Point out each leukocyte.
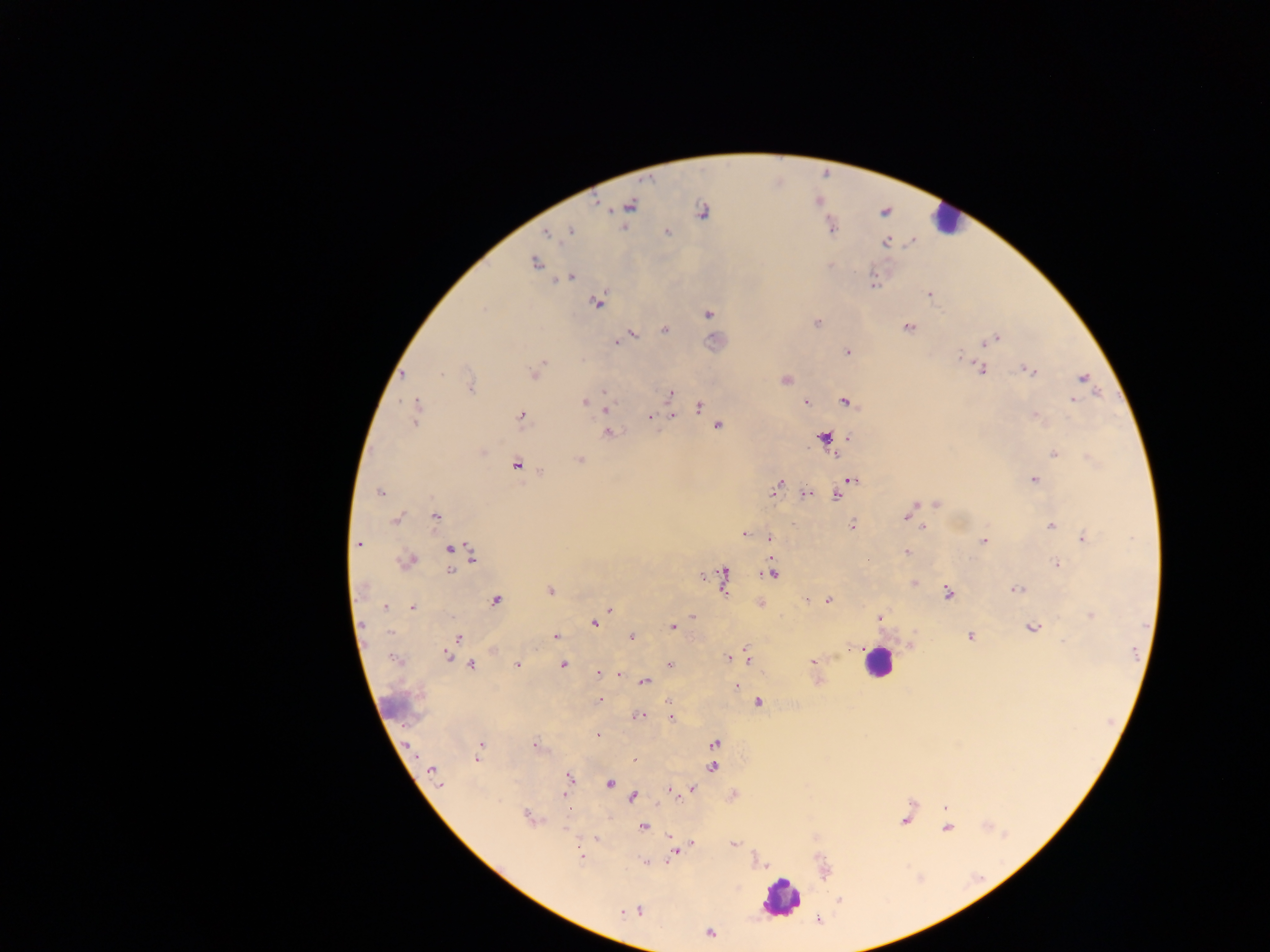

Approximate centers as {x, y} in pixels.
Leukocytes: {947, 219}, {878, 662}, {781, 897}.

Summary:
  - Malaria parasite locations: {596, 204}, {629, 205}, {701, 211}, {831, 226}, {570, 230}, {547, 231}, {667, 232}, {885, 241}, {912, 242}, {535, 262}, {570, 277}, {873, 283}, {930, 294}, {596, 302}, {708, 314}, {816, 323}, {907, 327}, {664, 329}, {631, 334}, {994, 338}, {621, 340}, {616, 342}, {984, 343}, {847, 352}, {979, 368}, {1027, 369}, {535, 372}, {1083, 378}, {785, 380}, {471, 386}, {605, 391}, {668, 394}, {1073, 400}, {806, 401}, {845, 401}, {583, 402}, {605, 406}, {698, 406}, {416, 411}, {521, 415}, {671, 415}, {1035, 416}, {650, 418}, {717, 426}, {607, 433}, {823, 438}, {848, 438}, {1053, 453}, {834, 454}, {579, 460}, {517, 463}, {850, 479}, {1033, 480}, {775, 487}, {379, 491}, {836, 493}, {805, 494}, {936, 503}, {912, 509}, {908, 515}, {435, 516}, {396, 518}, {852, 526}, {1050, 526}, {924, 528}, {743, 534}, {1083, 538}, {769, 539}, {984, 541}, {359, 543}, {451, 549}, {906, 551}, {473, 555}, {408, 560}, {1057, 564}, {451, 569}, {772, 572}, {723, 579}, {914, 582}, {1015, 589}, {550, 591}, {948, 592}, {496, 600}, {827, 600}, {760, 603}, {412, 606}, {383, 608}, {609, 609}, {1090, 615}, {693, 616}, {878, 617}, {594, 622}, {672, 627}, {1031, 627}, {556, 636}, {631, 636}, {970, 636}, {458, 638}, {909, 645}, {452, 647}, {447, 654}, {746, 656}, {728, 658}, {395, 660}, {814, 661}, {517, 664}, {670, 664}, {471, 665}, {562, 665}, {598, 673}, {617, 674}, {817, 679}, {644, 681}, {736, 686}, {599, 700}, {669, 701}, {759, 701}, {637, 716}, {671, 718}, {597, 735}, {714, 743}, {536, 746}, {480, 747}, {477, 755}, {635, 759}, {712, 766}, {432, 770}, {568, 779}, {609, 783}, {439, 785}, {691, 789}, {672, 792}, {733, 795}, {633, 797}, {945, 808}, {530, 817}, {904, 820}, {643, 826}, {946, 827}, {567, 829}, {670, 837}, {596, 838}, {692, 844}, {734, 844}, {675, 852}, {581, 857}, {644, 862}, {764, 865}, {623, 911}, {634, 911}, {818, 919}, {709, 932}
  - Preparation: thick blood smear
  - Field of view: single
  - Country: Ghana
  - Image size: 1270×952 pixels
  - Capture: mobile-phone photograph through a microscope